State which parasite is depicted.
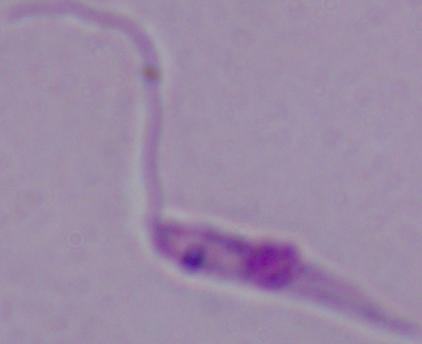
This is Leishmania.

Summary:
  - Magnification: 1000x
  - Modality: micrograph